Report the malaria status of this cell.
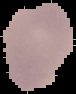
It is uninfected.

From a thin blood smear. Image is 76×94 pixels. Segmented cell region on a black background.